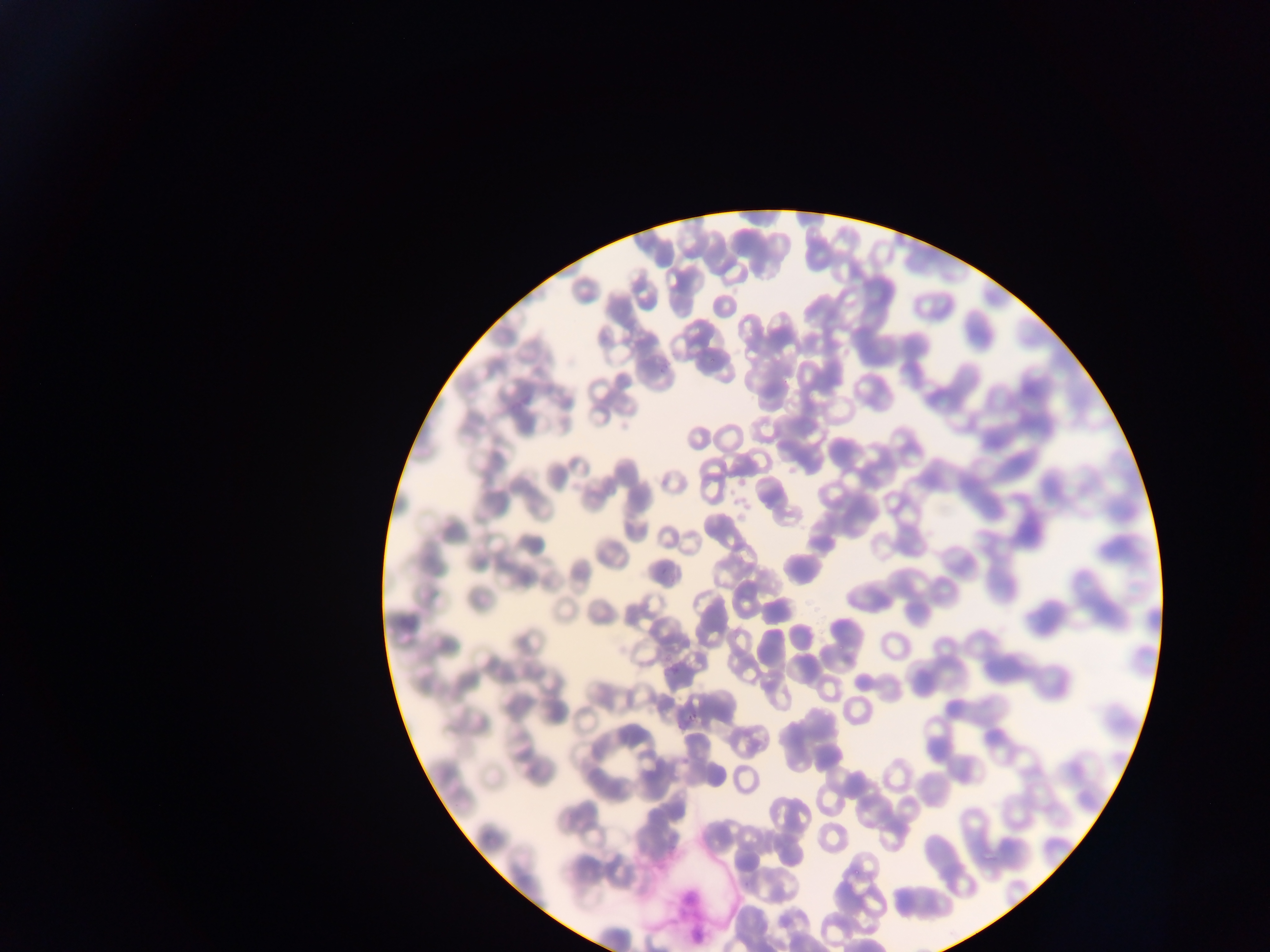

{
  "plasmodium_parasite_locations": "approximate bounding boxes as [left, top, right, bottom] in pixels: [655, 368, 667, 379], [666, 663, 686, 676], [685, 718, 697, 728]",
  "country": "Ghana",
  "preparation": "thin blood film",
  "capture": "mobile-phone photograph through a microscope",
  "image_size": "1270×952 pixels",
  "field_of_view": "single"
}